Describe the morphology of the erythrocytes.
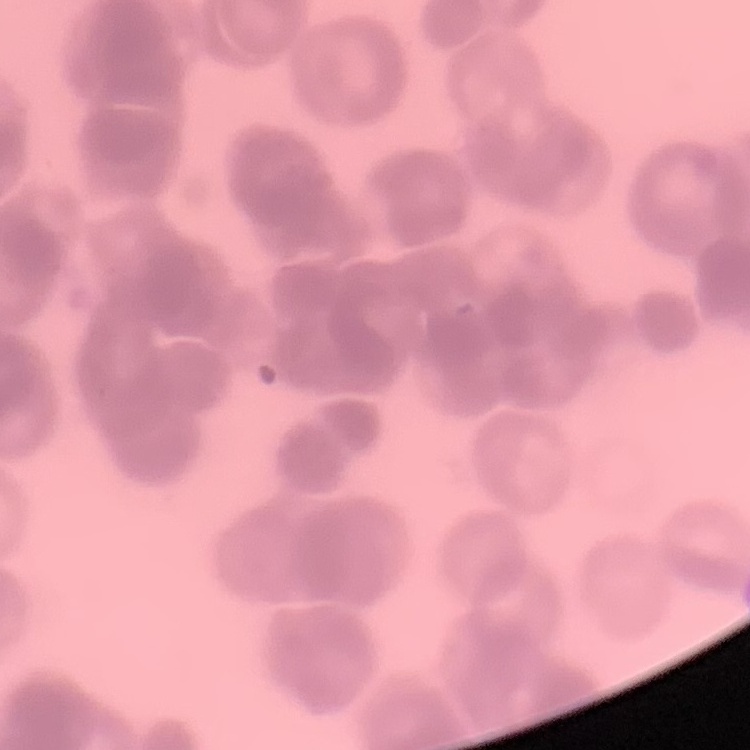
They show rouleaux formation.

image_type: square crop of a larger photomicrograph
stain: Field's or Giemsa
preparation: thin blood film